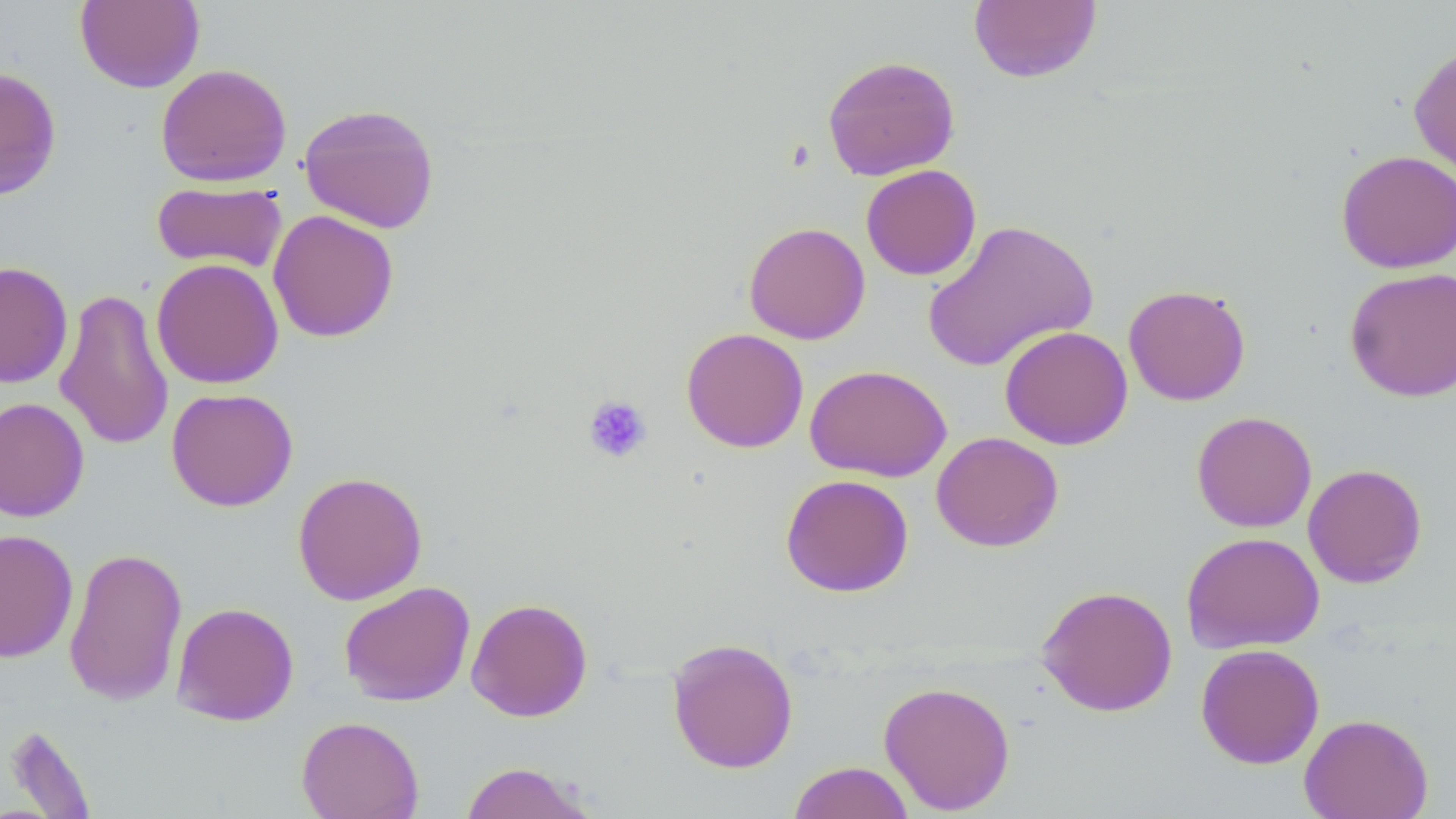
Approximate bounding boxes as [x1, y1, x2, y2] in pixels. Platelet locations: [583, 395, 652, 464]. Uninfected red blood cell locations: [968, 0, 1102, 84], [75, 1, 204, 93], [1408, 43, 1456, 184], [822, 55, 960, 181], [155, 63, 292, 187], [0, 66, 62, 201], [298, 102, 440, 234], [1335, 150, 1456, 273], [861, 164, 981, 280], [151, 181, 286, 273], [268, 209, 399, 343], [922, 219, 1099, 373], [743, 221, 871, 344], [151, 258, 284, 389], [0, 261, 73, 388], [1344, 266, 1456, 402], [1123, 284, 1251, 406], [55, 286, 174, 451], [999, 325, 1133, 450], [681, 327, 809, 453], [804, 364, 952, 482], [166, 388, 298, 511], [0, 397, 90, 522], [1191, 411, 1317, 532], [931, 431, 1064, 552], [1302, 463, 1427, 588], [292, 471, 428, 605], [780, 473, 914, 597], [0, 529, 78, 663], [1181, 531, 1325, 654], [63, 546, 187, 706], [338, 581, 476, 707], [1036, 585, 1178, 716], [466, 597, 593, 723], [172, 601, 299, 726], [666, 636, 799, 773], [1195, 643, 1325, 769], [878, 680, 1016, 815], [1299, 713, 1433, 819], [296, 715, 424, 819], [3, 724, 97, 817], [458, 761, 597, 818], [787, 761, 915, 819]. Slide-level diagnosis: no evidence of blood parasites. Captured at 1000x magnification. Image is 1456×819 pixels. Thin blood smear. May-Grünwald-Giemsa stain. One field of a larger specimen. Optical microscopy.